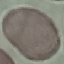 Malaria status: uninfected. Cell patch, automatically extracted from a larger field of view and resized to 64 × 64 pixels. Giemsa stain. Thin blood smear. Acquired by smartphone through the microscope eyepiece.